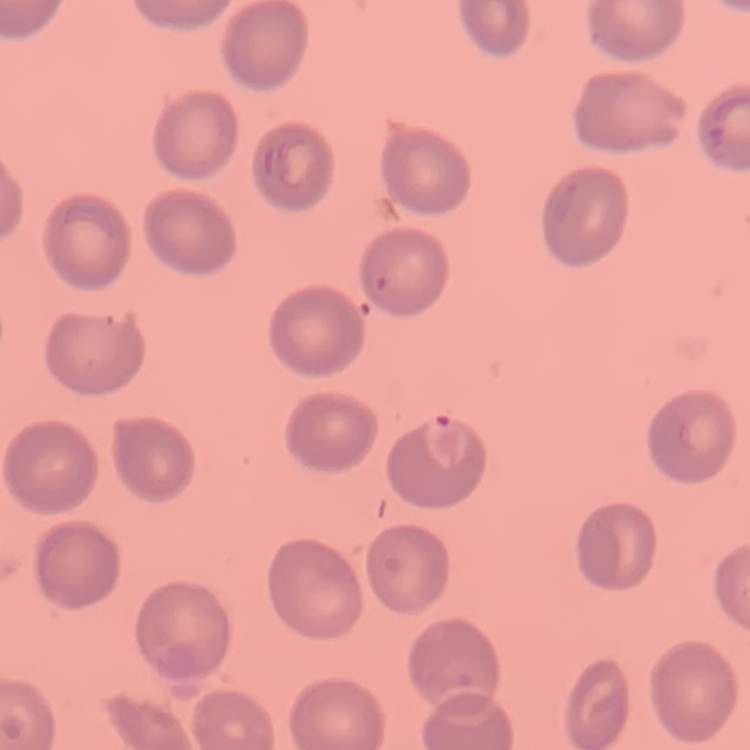 The red blood cells exhibit no rouleaux formation. One tile cut from a larger photomicrograph. Thin blood smear. Stained with either Field's or Giemsa.